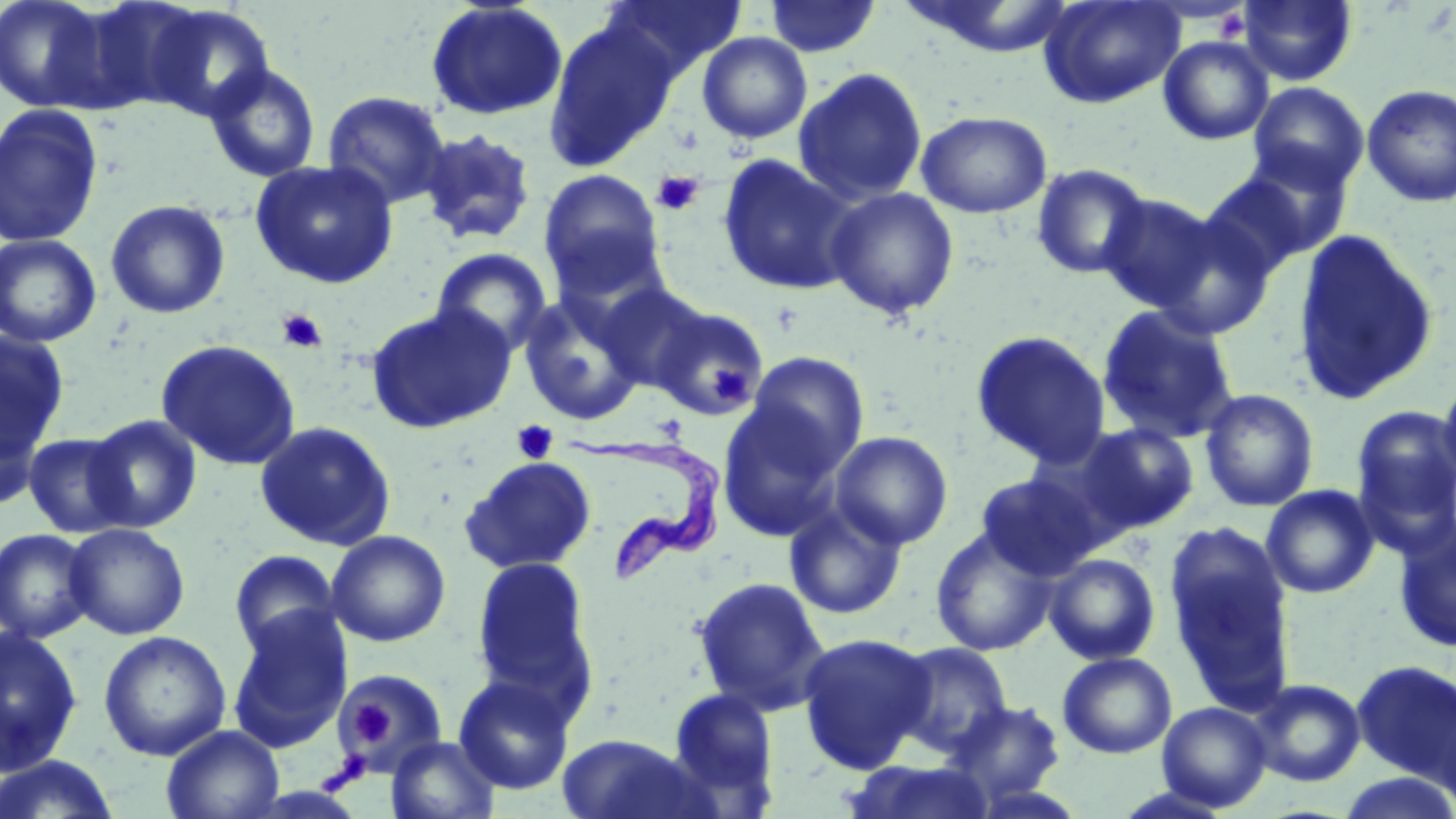
slide-level diagnosis = Trypanosoma brucei
platelet locations = approximate bounding boxes as (x1, y1, x2, y2) in pixels: (652, 170, 703, 217), (277, 309, 327, 353), (711, 366, 747, 402), (512, 419, 559, 464), (349, 701, 392, 747), (334, 751, 370, 790)
Trypanosoma brucei locations = approximate bounding boxes as (x1, y1, x2, y2) in pixels: (563, 434, 726, 582)
field of view = one of a larger specimen
magnification = 1000x
stain = May-Grünwald-Giemsa
uninfected red blood cell locations = approximate bounding boxes as (x1, y1, x2, y2) in pixels: (0, 0, 112, 113), (602, 0, 747, 79), (764, 0, 882, 58), (897, 0, 1081, 59), (1038, 0, 1186, 110), (1238, 1, 1357, 86), (425, 2, 568, 121), (140, 3, 277, 120), (542, 18, 679, 171), (697, 32, 812, 144), (1158, 35, 1274, 145), (204, 62, 321, 182), (793, 67, 928, 206), (1248, 82, 1369, 192), (1361, 83, 1456, 207), (322, 90, 451, 209), (0, 103, 105, 248), (916, 110, 1052, 218), (416, 128, 537, 247), (1208, 151, 1354, 274), (717, 153, 860, 296), (250, 160, 398, 289), (1030, 163, 1153, 280), (538, 168, 666, 297), (824, 187, 960, 320), (1096, 193, 1222, 312), (104, 199, 230, 319), (1146, 212, 1276, 341), (1292, 229, 1439, 407), (0, 234, 102, 348), (430, 248, 553, 356), (594, 281, 713, 394), (517, 290, 648, 425), (364, 303, 517, 435), (650, 305, 771, 420), (1096, 305, 1241, 445), (970, 329, 1111, 467), (0, 333, 70, 465), (156, 339, 302, 470), (744, 352, 870, 474), (1438, 374, 1456, 493), (1199, 388, 1319, 513), (0, 395, 47, 512), (717, 400, 848, 540), (1351, 406, 1456, 549), (85, 414, 202, 532), (255, 421, 397, 551), (1076, 422, 1200, 534), (830, 430, 953, 550), (22, 432, 135, 538), (460, 455, 597, 574), (975, 473, 1102, 580), (1261, 485, 1380, 598), (784, 501, 908, 620), (1393, 520, 1456, 653), (64, 523, 190, 640), (930, 526, 1058, 656), (0, 528, 97, 643), (326, 530, 451, 646), (1169, 542, 1296, 712), (228, 549, 342, 656), (1043, 553, 1160, 665), (471, 556, 597, 708), (693, 575, 832, 716), (227, 608, 352, 752), (0, 626, 83, 776), (98, 630, 232, 761), (797, 632, 935, 774), (890, 641, 1013, 757), (1058, 652, 1177, 758), (1352, 659, 1456, 783), (336, 667, 449, 776), (453, 673, 576, 794), (1248, 678, 1365, 787), (665, 687, 780, 810), (1426, 694, 1456, 811), (947, 699, 1067, 805), (1156, 702, 1271, 812), (161, 725, 285, 819), (555, 733, 720, 819), (385, 736, 501, 819), (1, 754, 123, 818), (842, 759, 999, 819), (1337, 772, 1456, 819)
image size = 1456×819 pixels
modality = optical microscopy
preparation = thin blood film